Identify the blood parasite species.
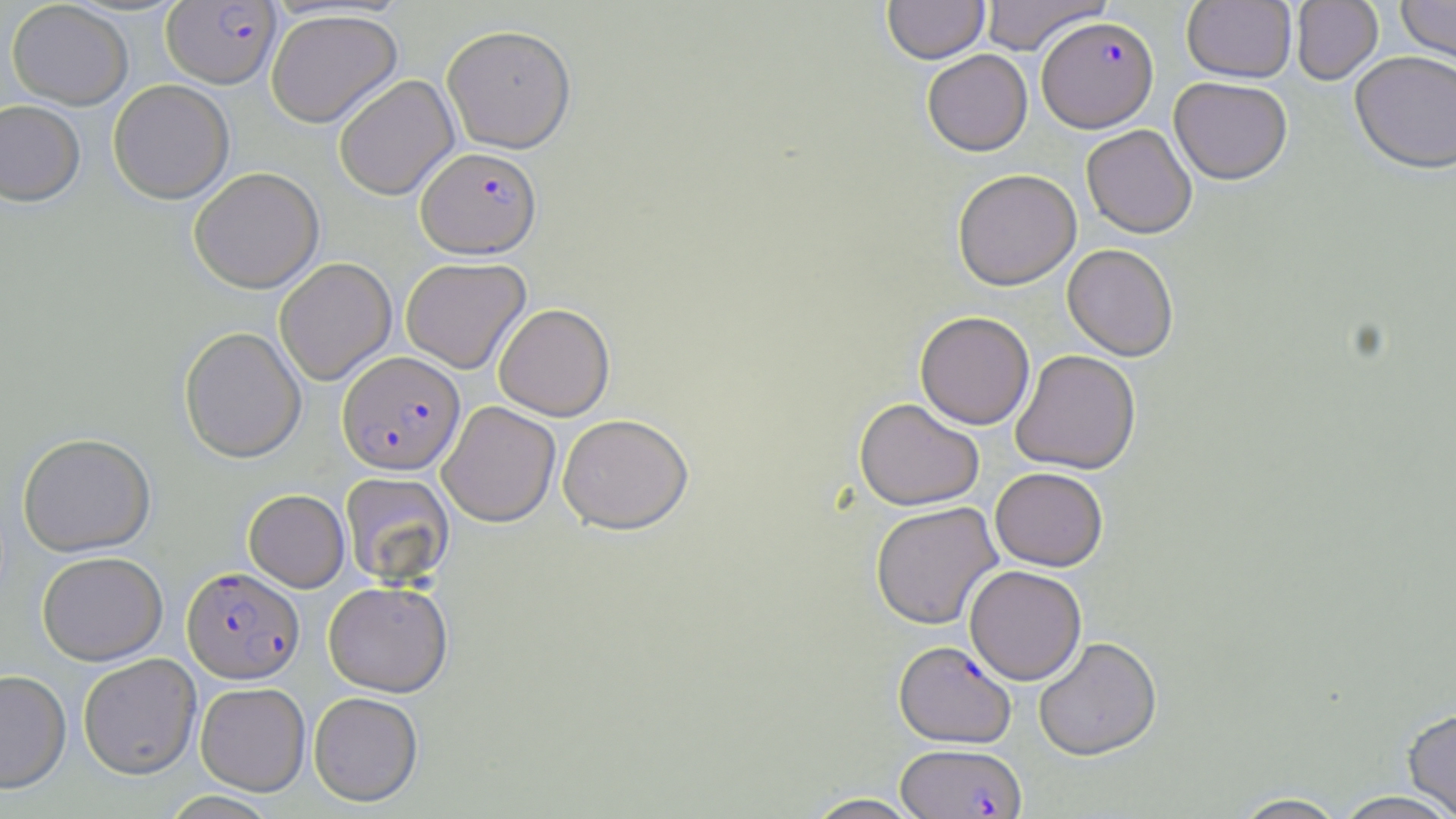

Plasmodium falciparum.

Approximate bounding boxes as (x1,y1)-(x2,y2) corner pairs in pixels. Uninfected red blood cell locations: (882,0)-(989,63), (979,0)-(1110,55), (1396,0)-(1456,71), (6,1)-(133,109), (1182,1)-(1296,83), (1291,1)-(1383,84), (266,8)-(402,128), (442,24)-(576,153), (922,49)-(1032,156), (1350,50)-(1456,173), (333,74)-(459,200), (1169,76)-(1292,184), (108,79)-(234,204), (0,100)-(85,205), (1081,124)-(1197,238), (189,167)-(324,293), (952,168)-(1081,291), (1062,244)-(1179,360), (274,257)-(396,385), (400,257)-(531,373), (493,303)-(614,420), (915,311)-(1035,429), (179,326)-(306,463), (1011,349)-(1141,474), (854,397)-(984,510), (438,401)-(561,527), (557,413)-(693,534), (17,432)-(156,556), (990,467)-(1108,571), (340,471)-(454,587), (243,489)-(349,592), (870,501)-(1002,629), (36,551)-(167,665), (964,565)-(1087,685), (323,580)-(453,696), (1033,636)-(1162,761), (77,653)-(201,779), (0,669)-(71,793), (195,682)-(310,795), (309,691)-(423,806), (1402,707)-(1456,818), (1333,790)-(1456,818), (801,792)-(925,818), (1231,792)-(1349,818). Plasmodium falciparum-infected red blood cell locations: (161,1)-(281,88), (1036,16)-(1158,131), (416,146)-(541,258), (338,350)-(465,475), (181,566)-(304,683), (894,640)-(1016,747), (895,743)-(1027,818). Thin blood film. Light microscopy. One field of a larger specimen. Image is 1456×819 pixels. 1000x magnification. May-Grünwald-Giemsa-stained preparation.